Assess this cell for malaria.
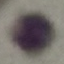
It is uninfected.

Giemsa stain. Automatically extracted cell patch, resized to 64 × 64 pixels. Photographed with a smartphone camera at the microscope eyepiece. Thin smear of blood.